Draw a bounding box around every malaria parasite.
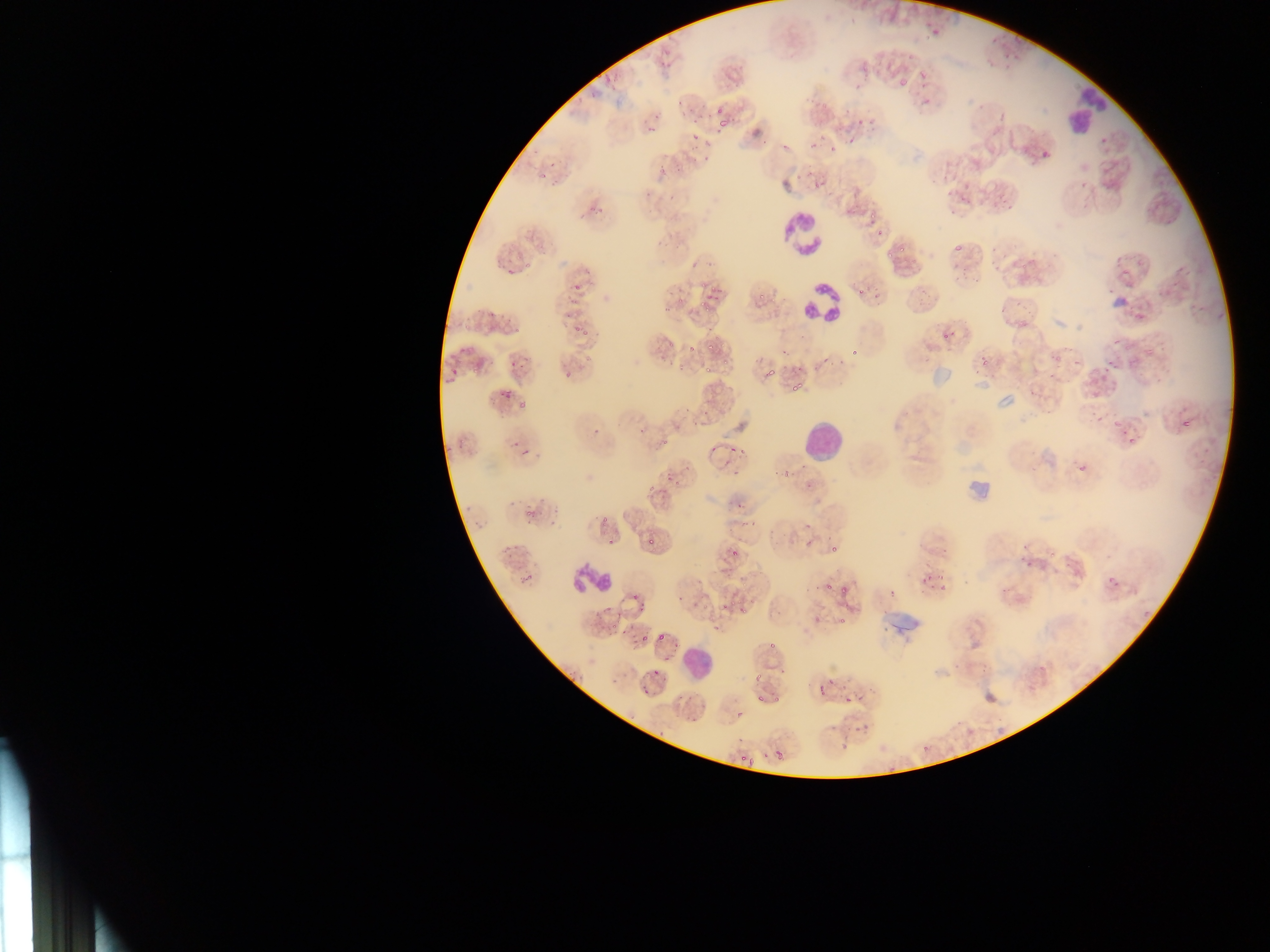
Approximate bounding boxes as {left, top, right, bottom} in pixels.
Malaria parasites: {929, 26, 940, 36}, {594, 68, 603, 80}, {918, 68, 927, 80}, {896, 71, 913, 86}, {606, 76, 615, 84}, {714, 104, 738, 129}, {854, 115, 867, 126}, {648, 124, 657, 133}, {846, 136, 857, 146}, {809, 139, 817, 148}, {781, 142, 789, 150}, {830, 146, 838, 153}, {703, 155, 712, 163}, {537, 157, 559, 180}, {657, 166, 668, 174}, {794, 172, 803, 181}, {812, 179, 823, 190}, {868, 207, 879, 219}, {876, 226, 884, 237}, {952, 240, 964, 256}, {886, 251, 894, 258}, {1021, 261, 1029, 269}, {1122, 267, 1133, 275}, {565, 276, 582, 295}, {699, 282, 707, 289}, {756, 283, 779, 302}, {710, 284, 721, 292}, {665, 285, 689, 317}, {854, 287, 864, 297}, {699, 293, 711, 310}, {567, 296, 577, 308}, {571, 318, 589, 335}, {513, 326, 520, 334}, {943, 331, 948, 339}, {706, 334, 720, 351}, {1111, 336, 1120, 345}, {657, 340, 670, 363}, {686, 343, 696, 354}, {849, 345, 861, 355}, {780, 347, 796, 361}, {1144, 349, 1154, 357}, {1053, 352, 1066, 362}, {721, 353, 727, 367}, {977, 357, 988, 369}, {822, 358, 831, 364}, {508, 360, 515, 368}, {763, 360, 778, 379}, {838, 360, 848, 370}, {1106, 361, 1117, 369}, {705, 362, 714, 373}, {811, 362, 822, 370}, {676, 363, 685, 372}, {791, 365, 808, 373}, {448, 367, 458, 374}, {469, 367, 483, 376}, {562, 373, 570, 380}, {790, 379, 804, 393}, {492, 390, 513, 404}, {516, 398, 531, 409}, {1179, 419, 1191, 430}, {1112, 421, 1122, 429}, {593, 428, 601, 436}, {1121, 430, 1128, 438}, {660, 437, 672, 446}, {1128, 438, 1138, 449}, {457, 439, 466, 447}, {510, 440, 518, 446}, {726, 442, 741, 464}, {740, 443, 747, 456}, {521, 446, 531, 456}, {710, 446, 717, 454}, {1077, 464, 1087, 473}, {783, 469, 791, 475}, {665, 471, 675, 483}, {806, 483, 815, 491}, {646, 485, 655, 493}, {731, 499, 743, 510}, {524, 509, 539, 517}, {751, 515, 758, 527}, {602, 517, 609, 525}, {740, 518, 748, 528}, {805, 524, 815, 529}, {645, 534, 656, 545}, {804, 539, 813, 554}, {501, 545, 513, 555}, {726, 546, 741, 559}, {1048, 549, 1056, 560}, {1107, 572, 1116, 582}, {520, 574, 532, 586}, {1112, 578, 1123, 590}, {823, 584, 831, 593}, {840, 587, 850, 595}, {1001, 587, 1008, 595}, {627, 594, 641, 602}, {676, 595, 684, 604}, {747, 597, 757, 609}, {719, 601, 734, 609}, {701, 604, 710, 610}, {601, 606, 613, 616}, {635, 606, 647, 616}, {737, 606, 748, 615}, {713, 622, 721, 632}, {608, 624, 623, 637}, {641, 632, 649, 642}, {656, 632, 672, 641}, {764, 638, 774, 651}, {566, 669, 581, 683}, {775, 669, 787, 679}, {753, 674, 762, 686}, {826, 679, 836, 685}, {818, 686, 826, 696}, {641, 688, 648, 696}, {854, 691, 863, 701}, {754, 693, 765, 707}, {844, 695, 852, 703}, {774, 696, 780, 706}, {735, 706, 748, 725}, {829, 724, 835, 732}, {854, 724, 862, 734}, {775, 750, 782, 758}, {748, 756, 757, 767}, {740, 757, 746, 765} | approximate {x, y} pixel centers of objects too small to bound: {693, 122}, {692, 138}, {597, 209}, {902, 251}, {1075, 362}, {677, 483}, {769, 532}, {612, 541}, {833, 549}, {940, 577}, {817, 619}, {843, 620}, {654, 672}, {661, 734}, {844, 746}.

Summary:
  - Leukocyte locations: {1058, 90, 1110, 133}, {791, 206, 836, 295}, {779, 211, 826, 258}, {802, 278, 852, 326}, {799, 285, 840, 321}, {802, 421, 842, 462}, {569, 563, 612, 594}, {679, 645, 714, 678}
  - Artifact (stain precipitate or debris) locations: {1109, 291, 1132, 311}, {928, 367, 949, 389}, {989, 392, 1017, 410}, {965, 461, 1000, 502}, {877, 595, 926, 633}
  - Field of view: single
  - Preparation: thin blood smear
  - Country: Ghana
  - Capture: mobile-phone photograph through a microscope
  - Image size: 1270×952 pixels